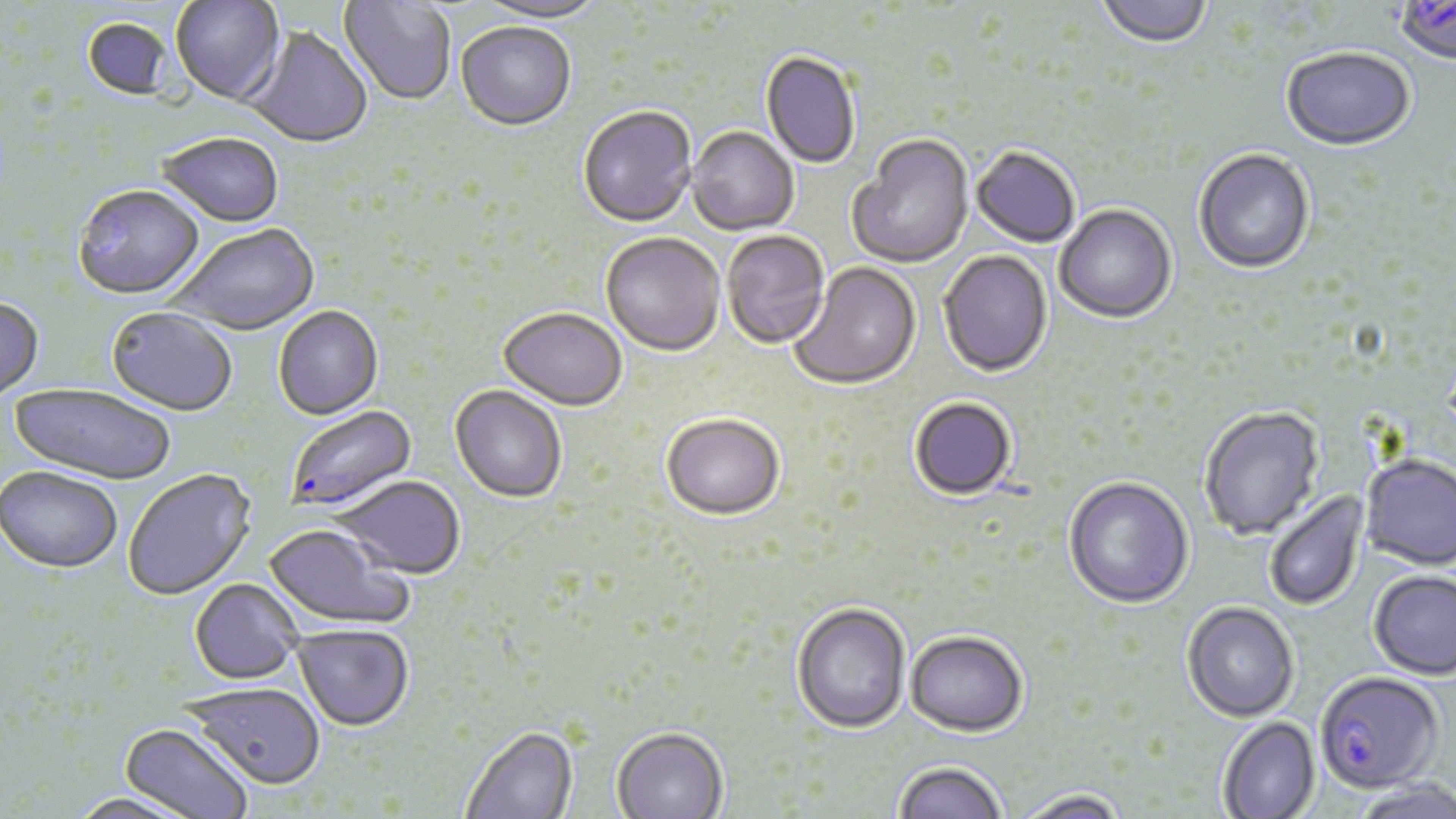
Summary:
  - Coordinate format: approximate bounding boxes as (x1, y1, x2, y2) in pixels
  - Uninfected red blood cell locations: (171, 0, 285, 106), (475, 0, 608, 27), (1097, 0, 1212, 51), (340, 1, 456, 107), (82, 19, 173, 101), (456, 23, 576, 133), (243, 27, 373, 150), (1281, 49, 1416, 153), (760, 53, 861, 170), (578, 108, 697, 230), (686, 128, 799, 237), (156, 134, 284, 229), (848, 136, 974, 270), (971, 148, 1081, 249), (1193, 150, 1315, 276), (73, 187, 204, 302), (1054, 206, 1177, 325), (169, 226, 319, 338), (722, 231, 830, 351), (600, 234, 725, 358), (938, 251, 1053, 379), (788, 262, 922, 392), (0, 298, 44, 402), (274, 307, 384, 421), (107, 308, 238, 417), (498, 310, 627, 413), (8, 382, 178, 486), (450, 386, 568, 504), (909, 398, 1017, 502), (1199, 407, 1326, 541), (661, 417, 785, 524), (1360, 456, 1456, 573), (0, 465, 122, 573), (122, 468, 256, 600), (334, 476, 466, 579), (1063, 478, 1194, 611), (1265, 490, 1369, 612), (263, 524, 414, 631), (1368, 572, 1456, 682), (190, 579, 303, 684), (791, 603, 912, 735), (1181, 604, 1299, 724), (293, 624, 414, 731), (905, 633, 1029, 740), (186, 682, 326, 789), (1218, 717, 1321, 818), (118, 722, 255, 819), (460, 725, 578, 819), (610, 728, 729, 818), (893, 763, 1007, 819), (1351, 781, 1456, 819), (64, 791, 205, 819), (1011, 791, 1132, 819)
  - Plasmodium falciparum-infected red blood cell locations: (1393, 2, 1456, 67), (286, 405, 418, 513), (1314, 674, 1443, 797)
  - Slide-level diagnosis: Plasmodium falciparum
  - Preparation: thin blood film
  - Stain: May-Grünwald-Giemsa
  - Field of view: single
  - Modality: optical microscopy
  - Image size: 1456×819 pixels
  - Magnification: 1000x